Classify this cell by malaria status.
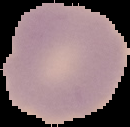
Uninfected.

Summary:
  - Image size: 130×127 pixels
  - Image type: cell region segmented out of the field of view; surrounding area masked to black
  - Preparation: thin blood smear